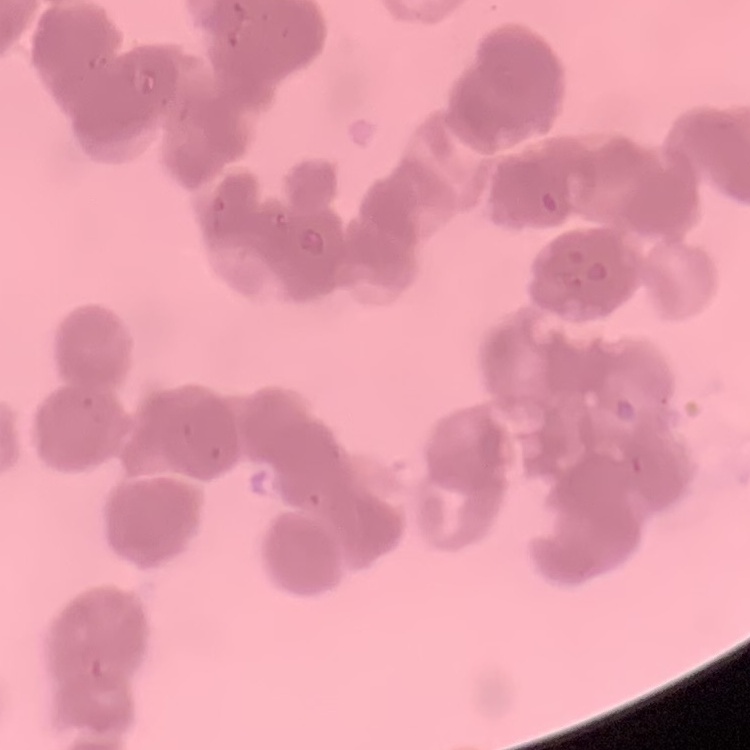
Summary:
  - Erythrocyte morphology: rouleaux formation
  - Image type: one tile cut from a larger photomicrograph
  - Preparation: thin peripheral smear
  - Stain: Field's or Giemsa